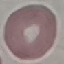

Result: no malaria parasites detected. Acquired by smartphone through the microscope eyepiece. Cell patch, automatically extracted from a larger field of view and resized to 64 × 64 pixels. Giemsa-stained preparation. Thin blood film.